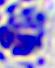 Captured at 400x magnification. A leukocyte is seen. Micrograph.